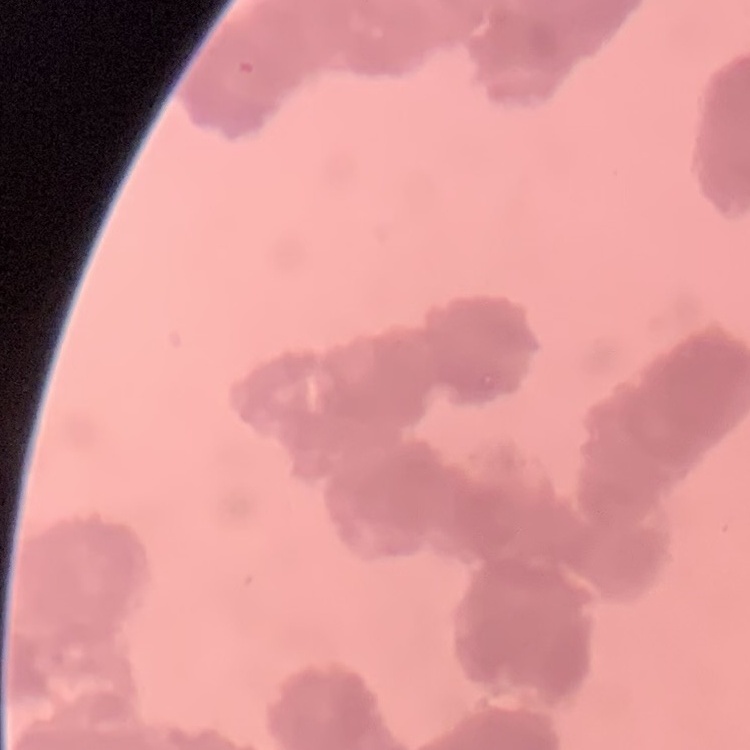

Summary:
  - Red blood cell morphology: rouleaux formation
  - Image type: square crop of a larger photomicrograph
  - Preparation: thin blood film
  - Stain: Field's or Giemsa